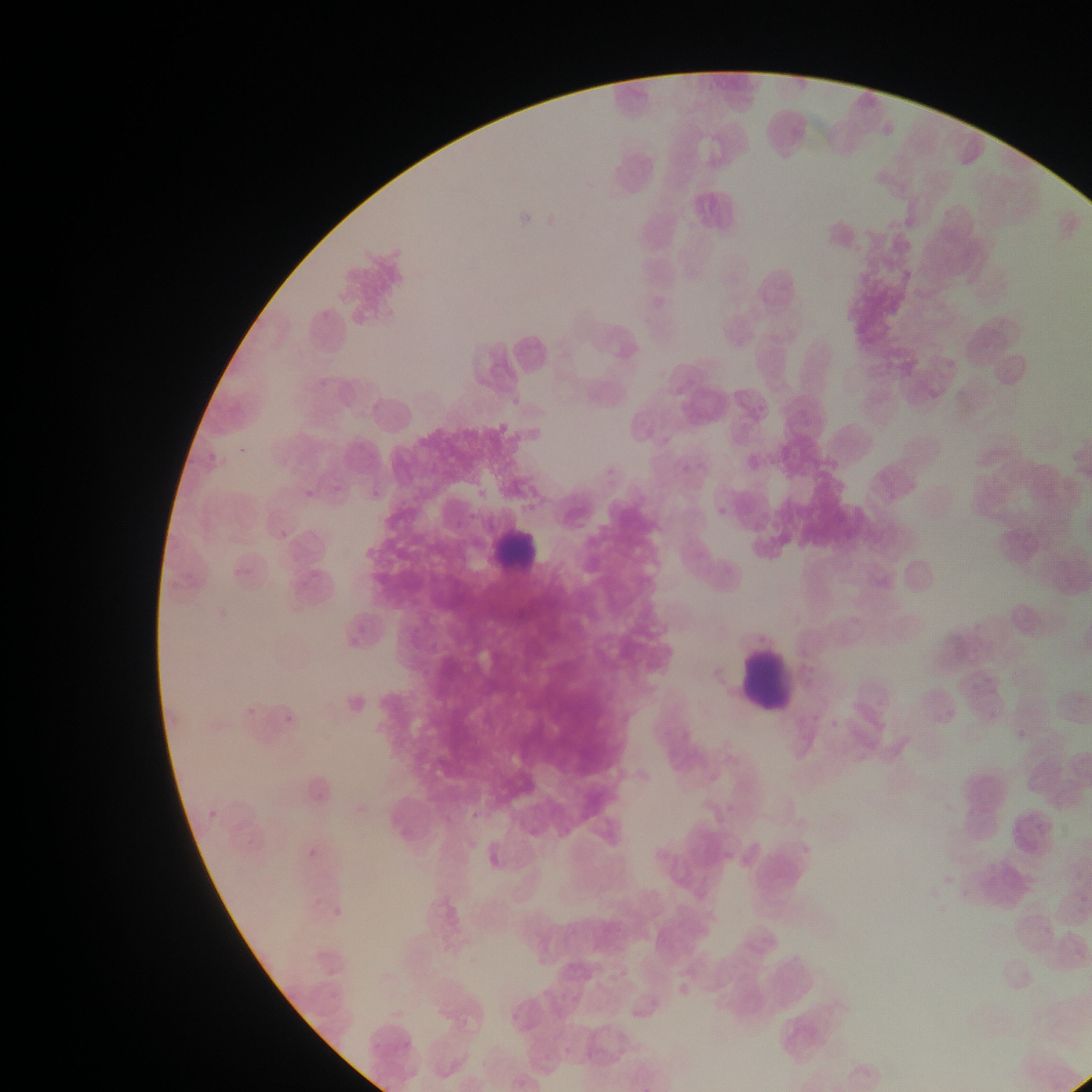 Approximate bounding boxes as [left, top, right, bottom] in pixels. Leukocyte locations: [489, 517, 553, 578], [737, 636, 801, 720]. Image is 1092×1092 pixels. Collected in Ghana. Thin blood film. Mobile-phone photograph taken through the microscope. One field of view.